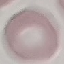
result = negative for malaria parasites
preparation = thin blood smear
image type = cell patch, automatically extracted from a larger field of view and resized to 64 × 64 pixels
capture = smartphone through the microscope eyepiece
stain = Giemsa